Outline each Trypanosoma brucei.
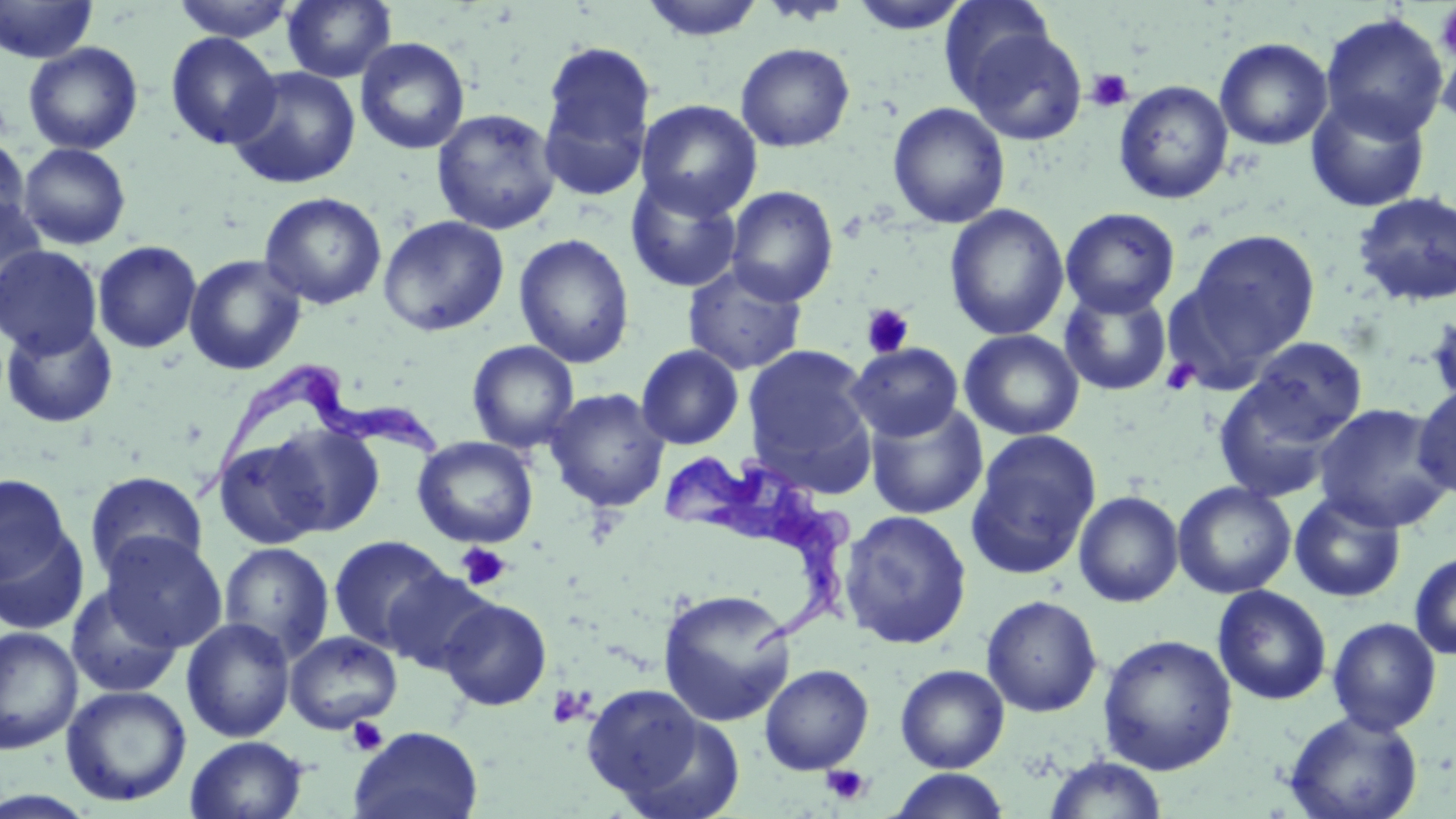
Approximate bounding boxes as (x1,y1)-(x2,y2) corner pairs in pixels.
Trypanosoma brucei: (178,354)-(444,501), (655,448)-(856,658).

Platelet locations: (1435,4)-(1456,61), (1085,69)-(1134,113), (861,303)-(914,358), (1160,358)-(1200,396), (455,542)-(512,591), (547,686)-(592,728), (346,715)-(388,756), (821,764)-(872,806). Uninfected red blood cell locations: (0,0)-(97,64), (171,0)-(298,41), (282,0)-(396,83), (639,0)-(767,42), (846,0)-(974,34), (939,0)-(1059,105), (1319,12)-(1449,142), (958,26)-(1088,145), (166,33)-(281,150), (354,37)-(471,155), (1214,37)-(1333,150), (1437,37)-(1456,136), (539,40)-(656,194), (23,42)-(143,155), (735,42)-(855,152), (228,66)-(361,189), (1114,80)-(1233,204), (1304,93)-(1431,213), (636,99)-(763,220), (887,102)-(1010,229), (431,108)-(560,235), (0,136)-(31,246), (18,143)-(131,250), (625,175)-(743,292), (725,186)-(838,306), (259,191)-(387,310), (1352,191)-(1456,307), (0,193)-(49,315), (944,203)-(1070,341), (1060,207)-(1180,317), (377,215)-(509,336), (1184,229)-(1320,366), (514,233)-(635,368), (92,240)-(202,353), (1,245)-(103,358), (184,253)-(306,375), (683,262)-(807,375), (1058,286)-(1172,397), (1425,307)-(1456,410), (0,319)-(119,428), (959,329)-(1085,440), (1243,337)-(1368,444), (467,340)-(579,453), (847,342)-(963,442), (636,344)-(744,450), (743,344)-(877,487), (1213,372)-(1348,502), (1412,384)-(1455,500), (544,388)-(670,511), (864,402)-(989,520), (1314,403)-(1454,532), (264,422)-(386,537), (966,430)-(1101,579), (212,436)-(332,549), (412,436)-(539,549), (85,471)-(208,579), (0,474)-(73,588), (1172,481)-(1296,598), (1072,490)-(1184,607), (1289,491)-(1407,602), (838,510)-(972,649), (0,520)-(90,636), (100,533)-(226,651), (328,535)-(455,655), (218,542)-(335,662), (1409,550)-(1456,661), (382,570)-(497,676), (65,584)-(183,698), (1212,585)-(1332,705), (657,588)-(796,727), (981,594)-(1102,717), (438,597)-(552,711), (181,617)-(296,743), (1327,617)-(1442,735), (0,626)-(83,754), (284,631)-(403,733), (1097,633)-(1238,775), (759,664)-(874,775), (895,664)-(1010,773), (581,684)-(717,807), (61,685)-(192,807), (1283,710)-(1423,819), (349,726)-(484,819), (185,736)-(308,819), (1042,755)-(1168,818), (889,769)-(1010,818), (0,789)-(99,818). Slide-level diagnosis: Trypanosoma brucei. Thin blood film. May-Grünwald-Giemsa stain. One field of a larger specimen. Optical microscopy. Image is 1456×819 pixels. Captured at 1000x magnification.